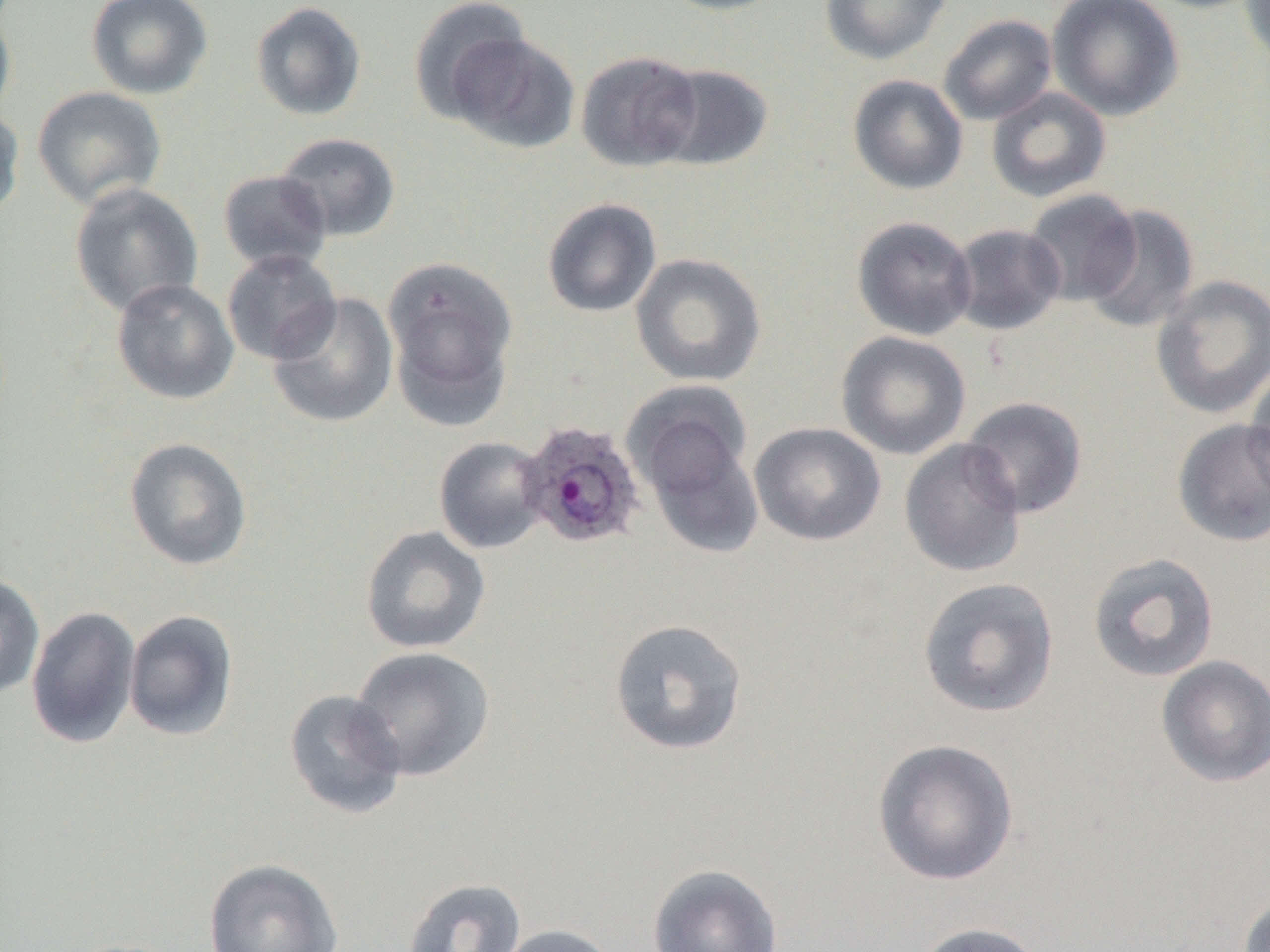

Summary:
  - Coordinate format: approximate bounding boxes as [x1, y1, x2, y2] in pixels
  - Plasmodium ovale-infected red blood cell locations: [519, 421, 645, 549]
  - Uninfected red blood cell locations: [85, 0, 214, 100], [408, 0, 536, 123], [651, 0, 790, 16], [819, 0, 951, 65], [1046, 0, 1184, 122], [1138, 0, 1267, 13], [1239, 0, 1270, 70], [249, 1, 367, 122], [0, 4, 17, 128], [938, 14, 1058, 125], [446, 32, 579, 154], [576, 51, 703, 172], [654, 63, 774, 172], [847, 74, 969, 195], [31, 86, 167, 209], [986, 87, 1112, 203], [0, 104, 25, 224], [274, 132, 401, 242], [218, 170, 332, 273], [69, 182, 205, 317], [1022, 189, 1142, 306], [542, 198, 662, 318], [1081, 205, 1199, 334], [851, 216, 977, 341], [949, 223, 1067, 336], [221, 249, 342, 365], [630, 253, 767, 387], [382, 256, 519, 427], [1150, 274, 1270, 420], [111, 278, 239, 405], [267, 292, 399, 429], [836, 330, 971, 460], [1245, 358, 1270, 506], [625, 383, 760, 538], [961, 396, 1088, 519], [1171, 418, 1270, 547], [749, 422, 886, 546], [433, 436, 550, 554], [123, 437, 253, 571], [899, 438, 1027, 578], [360, 525, 491, 654], [1087, 552, 1220, 683], [0, 573, 45, 699], [917, 577, 1060, 718], [26, 606, 141, 749], [123, 610, 239, 741], [608, 618, 748, 756], [349, 646, 496, 782], [1155, 655, 1270, 788], [283, 689, 408, 819], [872, 738, 1019, 886], [203, 857, 343, 952], [647, 862, 783, 952], [401, 877, 527, 952], [1237, 891, 1270, 952], [911, 921, 1048, 952], [493, 923, 620, 952], [60, 938, 188, 952]
  - Slide-level diagnosis: Plasmodium ovale
  - Image size: 1270×952 pixels
  - Magnification: 1000x
  - Modality: optical microscopy
  - Preparation: thin blood film
  - Field of view: one of a larger specimen